Report the malaria status of this cell.
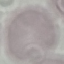

It is uninfected.

Summary:
  - Capture: smartphone through the microscope eyepiece
  - Stain: Giemsa
  - Preparation: thin smear
  - Image type: automatically extracted cell patch, resized to 64 × 64 pixels